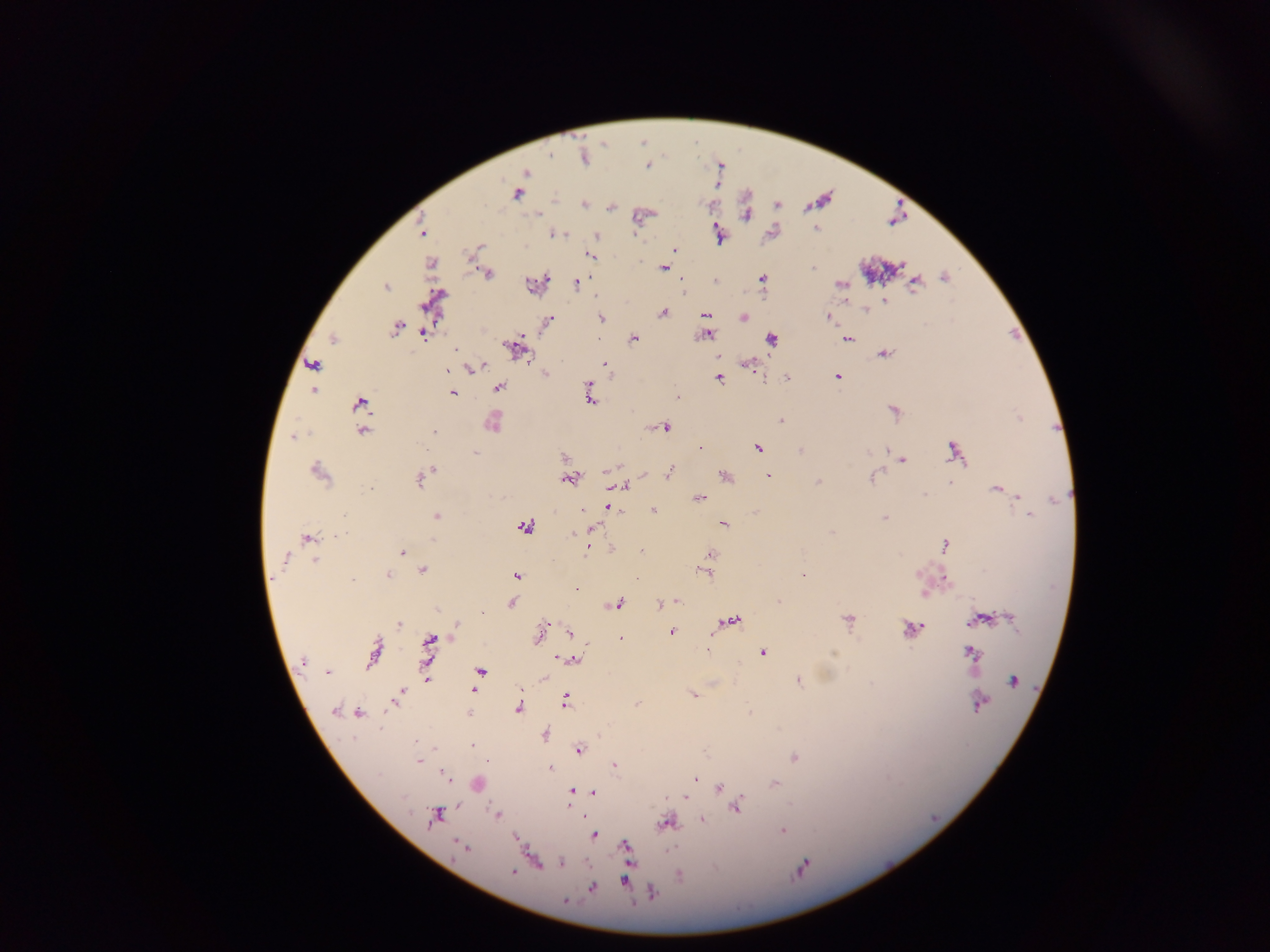

preparation = thick blood smear
country = Ghana
image size = 1270×952 pixels
Plasmodium parasite locations = approximate centers as (x, y) in pixels: (584, 157), (647, 166), (526, 172), (517, 193), (583, 204), (816, 228), (422, 233), (555, 234), (718, 235), (597, 236), (478, 247), (675, 250), (589, 255), (431, 262), (662, 268), (813, 268), (488, 274), (762, 278), (681, 280), (716, 281), (577, 283), (531, 284), (840, 284), (916, 284), (385, 287), (885, 301), (866, 310), (663, 314), (706, 315), (828, 317), (601, 318), (743, 318), (547, 322), (396, 328), (424, 333), (707, 335), (634, 338), (333, 340), (772, 340), (847, 340), (514, 348), (455, 349), (885, 354), (606, 363), (746, 363), (312, 364), (483, 365), (471, 368), (447, 370), (545, 373), (837, 376), (719, 378), (786, 378), (589, 385), (498, 387), (313, 390), (453, 393), (677, 398), (591, 400), (361, 402), (780, 421), (493, 423), (665, 427), (363, 431), (435, 432), (294, 436), (701, 447), (758, 449), (800, 450), (886, 450), (475, 453), (954, 453), (564, 457), (903, 461), (432, 468), (607, 471), (318, 472), (426, 472), (669, 473), (726, 476), (768, 476), (420, 479), (570, 479), (872, 479), (818, 482), (950, 483), (622, 485), (370, 489), (996, 489), (924, 494), (699, 498), (609, 507), (582, 510), (616, 510), (653, 510), (1025, 510), (1029, 515), (436, 516), (885, 518), (724, 524), (524, 526), (591, 529), (832, 532), (575, 534), (337, 536), (307, 539), (433, 540), (945, 545), (587, 550), (641, 551), (402, 552), (710, 554), (286, 558), (315, 560), (423, 571), (705, 572), (388, 576), (517, 576), (803, 576), (636, 578), (945, 578), (352, 580), (923, 594), (778, 601), (678, 602), (512, 603), (616, 604), (660, 604), (482, 613), (1012, 617), (848, 619), (978, 620), (732, 621), (398, 624), (544, 624), (456, 625), (543, 629), (911, 629), (671, 631), (569, 632), (538, 636), (621, 638), (430, 640), (374, 652), (763, 652), (972, 654), (559, 658), (573, 659), (303, 660), (426, 663), (480, 671), (328, 672), (426, 678), (544, 678), (1013, 681), (799, 682), (473, 690), (521, 691), (400, 694), (693, 695), (395, 699), (566, 701), (636, 704), (981, 704), (518, 708), (334, 711), (749, 712), (359, 714), (470, 714), (545, 734), (471, 746), (435, 749), (579, 750), (794, 757), (418, 760), (615, 765), (550, 769), (444, 775), (379, 776), (695, 779), (774, 784), (719, 787), (572, 791), (725, 791), (594, 793), (403, 797), (685, 798), (736, 807), (496, 814), (435, 817), (701, 819), (666, 822), (782, 831), (594, 835), (516, 836), (457, 843), (461, 846), (626, 846), (562, 863), (513, 872), (679, 876), (625, 881), (592, 888), (652, 893), (565, 901)
capture = mobile-phone photograph through a microscope
field of view = single